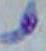

Toxoplasma gondii is shown. Micrograph. Captured at 1000x magnification.